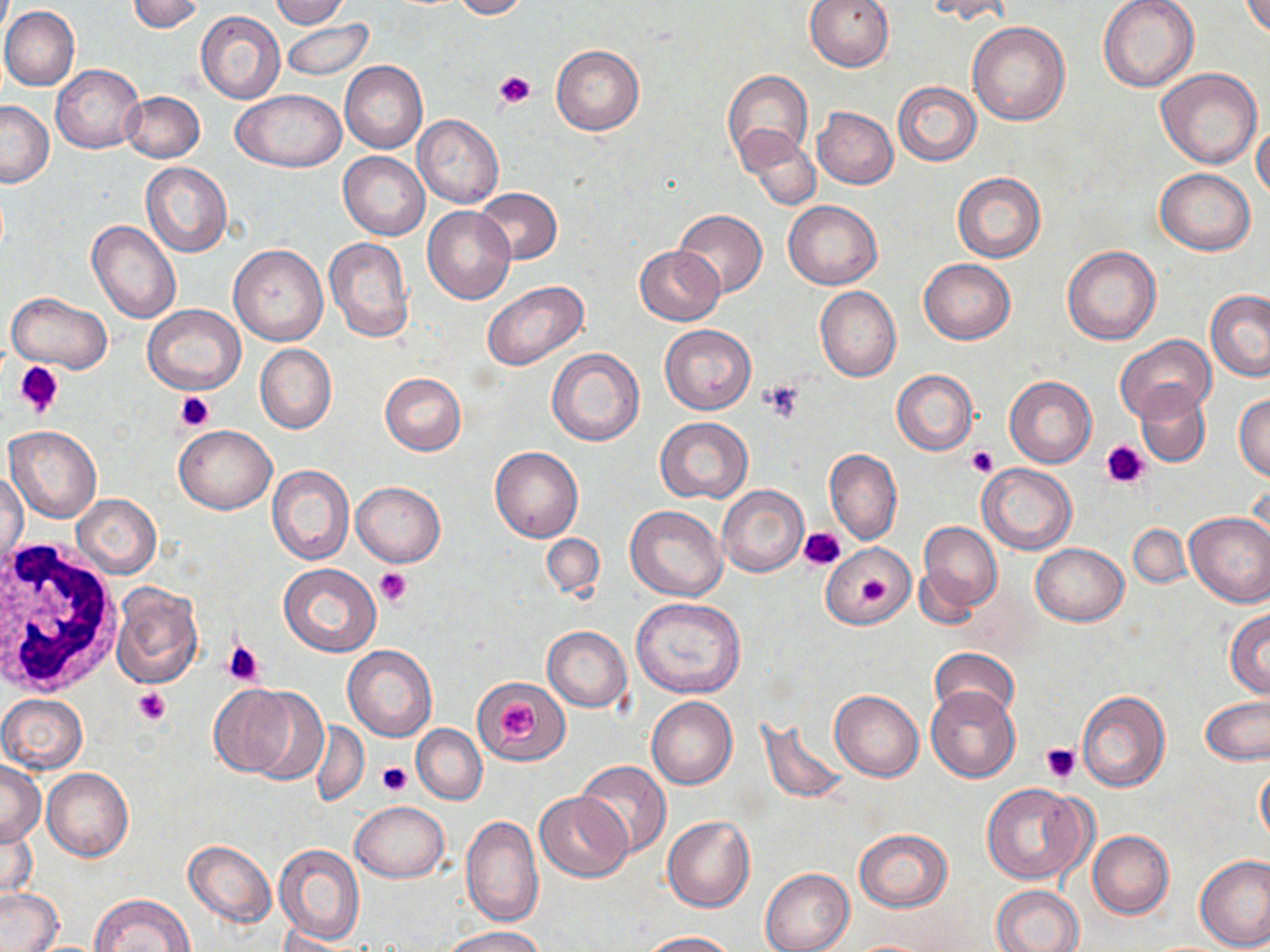
Approximate bounding boxes as (x1,y1)-(x2,y2) corner pairs in pixels. White blood cell locations: (0,539)-(121,699). Platelet locations: (493,70)-(534,109), (13,360)-(65,418), (760,380)-(803,422), (175,391)-(216,430), (1099,439)-(1153,490), (966,445)-(998,476), (798,526)-(845,571), (374,567)-(413,605), (223,641)-(264,687), (133,686)-(173,725), (500,701)-(537,745), (1040,743)-(1081,783), (377,761)-(412,797). Uninfected red blood cell locations: (127,0)-(203,35), (271,0)-(348,28), (451,0)-(529,19), (804,0)-(895,70), (922,0)-(1013,24), (1098,0)-(1199,91), (1239,0)-(1270,38), (1,7)-(79,91), (196,10)-(286,104), (202,15)-(372,94), (280,19)-(373,82), (968,21)-(1070,126), (551,45)-(644,135), (340,61)-(428,153), (51,63)-(144,152), (1158,68)-(1262,168), (723,70)-(813,167), (893,81)-(982,167), (232,88)-(346,172), (122,90)-(204,162), (0,99)-(53,188), (812,107)-(897,189), (412,115)-(504,208), (1252,123)-(1270,202), (736,128)-(820,212), (339,151)-(429,240), (141,163)-(232,257), (1154,168)-(1255,254), (951,172)-(1046,263), (475,187)-(562,264), (783,200)-(881,289), (422,206)-(516,305), (673,210)-(768,297), (87,221)-(181,325), (325,238)-(413,342), (229,243)-(327,345), (635,245)-(724,325), (1062,246)-(1160,346), (919,258)-(1015,344), (480,280)-(588,372), (814,287)-(901,381), (6,290)-(112,372), (1205,290)-(1270,382), (143,304)-(246,394), (660,325)-(755,414), (1114,335)-(1216,423), (255,343)-(337,433), (547,347)-(645,446), (891,370)-(978,454), (379,373)-(467,455), (1005,376)-(1097,467), (1135,384)-(1210,468), (1234,392)-(1270,481), (655,418)-(752,503), (5,424)-(102,523), (174,426)-(276,514), (491,447)-(583,542), (825,449)-(901,544), (975,463)-(1077,554), (266,464)-(354,566), (1,471)-(28,572), (1249,477)-(1269,562), (352,481)-(445,566), (718,485)-(809,577), (72,493)-(162,578), (625,505)-(726,601), (1185,512)-(1270,607), (917,522)-(1002,615), (1127,524)-(1190,590), (541,533)-(605,602), (823,541)-(914,629), (1031,542)-(1128,626), (278,564)-(380,657), (111,584)-(203,688), (630,597)-(746,698), (1225,609)-(1270,698), (542,625)-(631,712), (343,646)-(437,741), (928,646)-(1019,723), (474,677)-(568,765), (209,685)-(315,777), (925,686)-(1020,783), (830,689)-(924,781), (1075,689)-(1169,792), (0,693)-(88,774), (646,696)-(738,790), (1201,697)-(1270,766), (757,717)-(848,804), (311,721)-(368,805), (412,724)-(487,805), (1,760)-(46,846), (575,762)-(671,858), (1256,767)-(1270,846), (42,768)-(133,860), (983,782)-(1089,884), (534,792)-(632,882), (351,801)-(448,882), (461,815)-(544,928), (662,815)-(755,912), (2,819)-(38,899), (855,828)-(952,912), (1088,829)-(1174,919), (184,840)-(277,927), (274,843)-(366,946), (1195,853)-(1270,951), (760,868)-(854,952), (0,886)-(63,951), (991,886)-(1084,952), (90,892)-(195,952), (444,926)-(546,952), (639,930)-(739,951), (841,939)-(941,951). Slide-level diagnosis: negative for blood parasites. Thin blood smear. Optical microscopy. 1000x magnification. May-Grünwald-Giemsa-stained preparation. Image is 1270×952 pixels. Single field of view.